Classify this cell by malaria status.
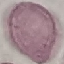
It is uninfected.

Acquired by smartphone through the microscope eyepiece. Cell patch, automatically extracted from a larger field of view and resized to 64 × 64 pixels. Giemsa-stained preparation. Thin blood smear.